Locate every uninfected red blood cell.
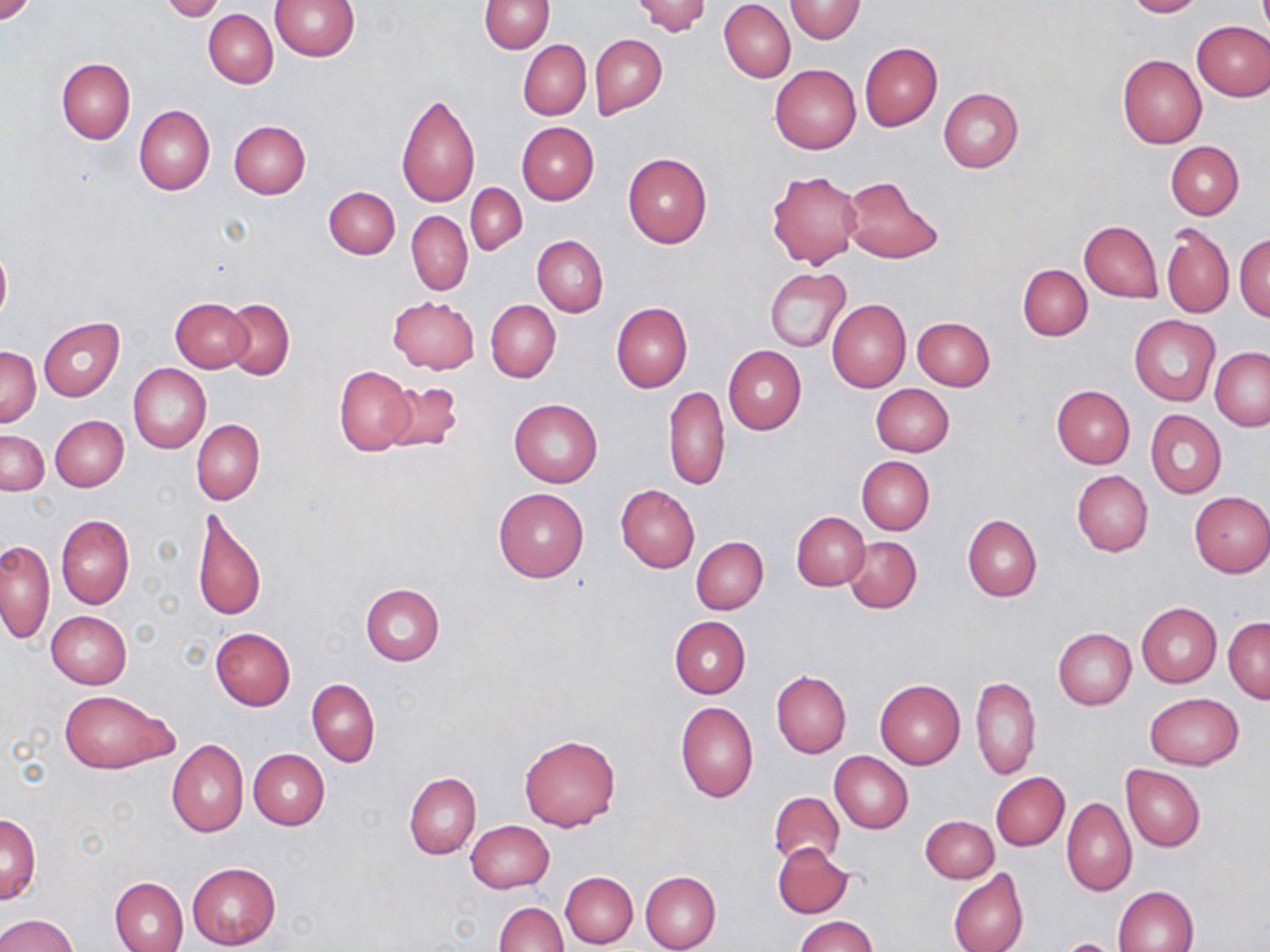
Approximate bounding boxes as (x1,y1)-(x2,y2) corner pairs in pixels.
Uninfected red blood cells: (0,0)-(36,24), (270,0)-(358,61), (480,0)-(553,53), (628,0)-(712,36), (785,0)-(865,42), (1121,0)-(1205,17), (161,1)-(227,21), (719,2)-(795,82), (203,6)-(357,76), (204,9)-(278,88), (1192,21)-(1270,100), (591,35)-(667,117), (518,40)-(591,120), (860,43)-(942,130), (1117,53)-(1207,148), (57,57)-(135,144), (770,65)-(860,154), (939,88)-(1023,172), (395,91)-(481,209), (135,105)-(214,195), (229,120)-(311,198), (517,122)-(599,204), (1166,142)-(1244,219), (622,153)-(712,248), (766,170)-(861,269), (840,177)-(943,263), (467,184)-(527,255), (323,185)-(400,259), (407,210)-(472,295), (1080,220)-(1162,302), (1162,224)-(1234,319), (1236,233)-(1270,321), (533,235)-(607,316), (0,243)-(11,324), (1019,264)-(1092,341), (764,268)-(851,353), (387,296)-(479,374), (171,297)-(252,372), (222,298)-(295,380), (827,299)-(910,392), (487,301)-(560,382), (611,303)-(693,392), (1130,315)-(1219,407), (39,317)-(125,402), (913,317)-(995,391), (723,345)-(806,435), (2,347)-(40,427), (1210,347)-(1270,430), (128,363)-(210,454), (334,366)-(415,456), (381,381)-(463,456), (871,383)-(954,457), (663,384)-(730,492), (1051,385)-(1136,468), (509,398)-(603,487), (1146,409)-(1226,497), (51,415)-(129,492), (192,420)-(263,505), (1,430)-(49,497), (857,455)-(934,535), (1073,470)-(1152,556), (616,484)-(699,573), (494,489)-(589,582), (1188,491)-(1270,577), (194,507)-(266,623), (791,511)-(869,591), (56,515)-(134,609), (963,515)-(1041,602), (845,536)-(922,613), (692,537)-(768,614), (1,540)-(55,643), (360,584)-(444,665), (1136,603)-(1221,688), (47,611)-(131,689), (669,615)-(750,697), (1223,618)-(1270,703), (210,627)-(296,711), (1053,627)-(1136,709), (772,669)-(851,758), (971,676)-(1041,780), (307,678)-(380,766), (875,680)-(965,769), (58,689)-(176,773), (1144,692)-(1243,769), (676,701)-(758,803), (519,734)-(620,832), (168,740)-(249,837), (248,749)-(329,829), (830,752)-(914,832), (1121,764)-(1205,851), (404,772)-(480,859), (991,772)-(1069,851), (769,790)-(844,867), (1062,797)-(1137,896), (1,814)-(40,905), (920,815)-(998,883), (466,820)-(554,892), (773,842)-(854,918), (186,862)-(280,949), (948,868)-(1028,952), (561,871)-(638,948), (640,871)-(720,952), (109,876)-(189,952), (1114,885)-(1199,952), (495,901)-(567,952), (0,914)-(79,952), (793,915)-(877,952).

Slide-level diagnosis: no evidence of blood parasites. Image is 1270×952 pixels. 1000x magnification. Single field of view. May-Grünwald-Giemsa stain. Thin blood film. Optical microscopy.